Identify the parasite.
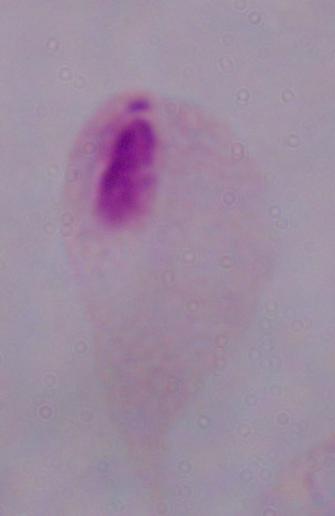

This is a trichomonad.

{
  "magnification": "1000x",
  "modality": "photomicrograph"
}